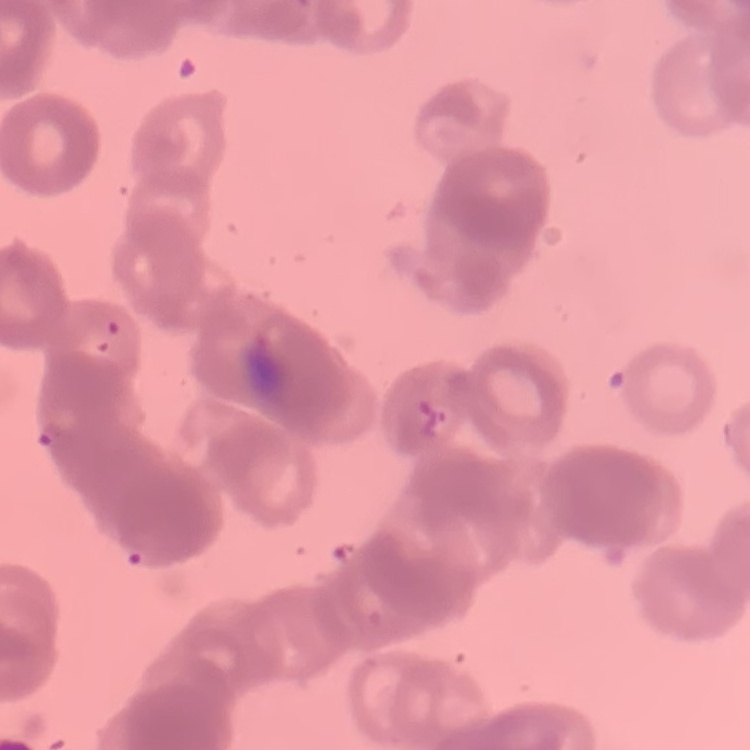

The red blood cells exhibit rouleaux formation. Thin blood film. One tile cut from a larger photomicrograph. Stained with either Field's or Giemsa.